Assess this cell for malaria.
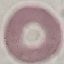

It is uninfected.

Summary:
  - Capture: smartphone camera at the microscope eyepiece
  - Image type: cell patch, automatically extracted from a larger field of view and resized to 64 × 64 pixels
  - Stain: Giemsa
  - Preparation: thin blood smear